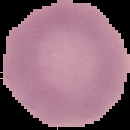
Summary:
  - Result: negative for Plasmodium parasites
  - Image size: 130×130 pixels
  - Preparation: thin blood film
  - Image type: segmented cell region on a black background